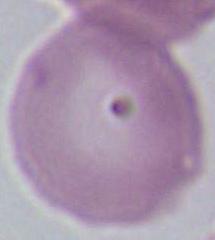

modality = micrograph
identification = erythrocyte
magnification = 1000x